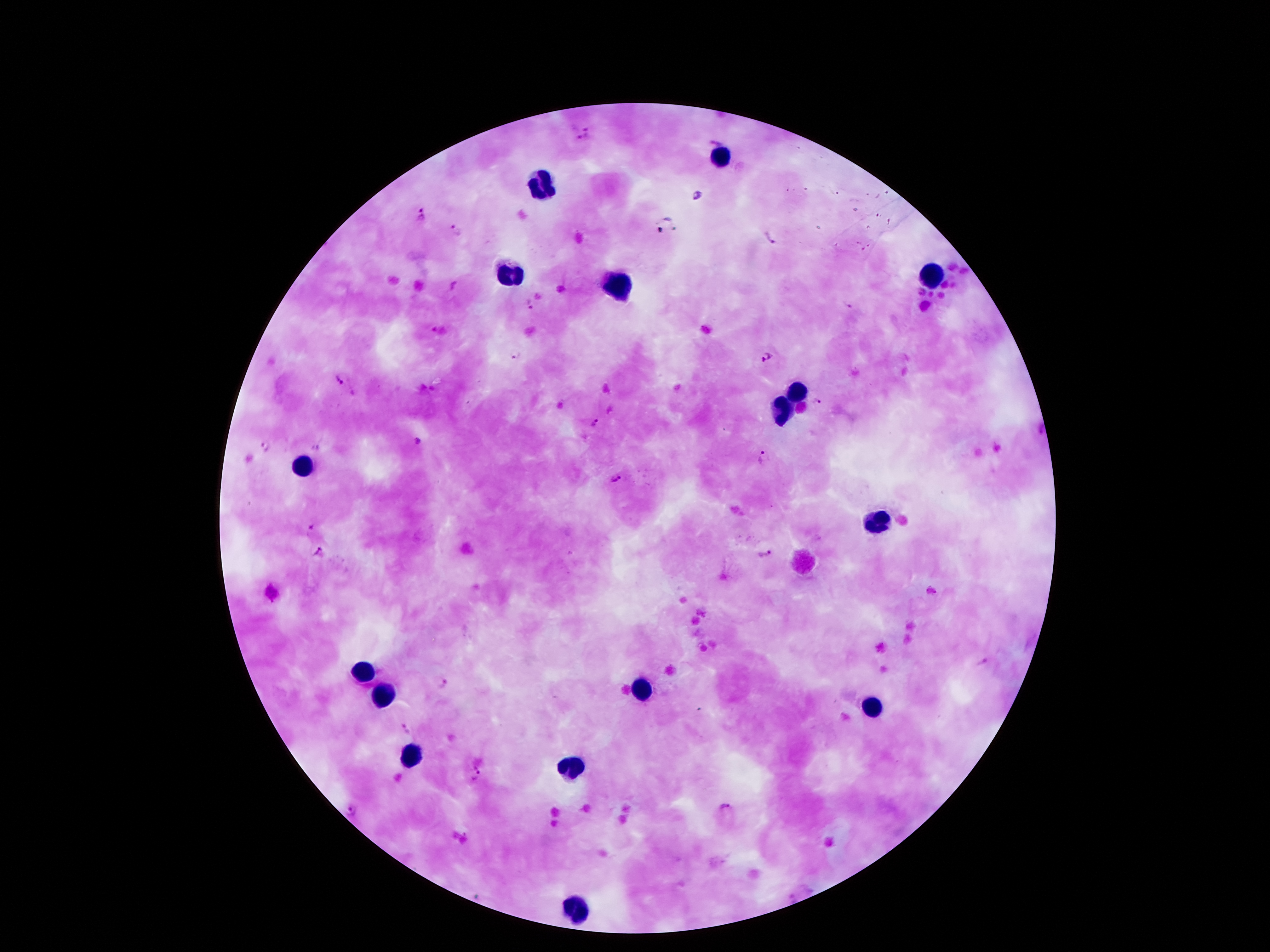
Approximate centers as (x, y) in pixels. Malaria parasite locations: (590, 131), (574, 134), (716, 141), (697, 197), (421, 216), (456, 232), (769, 239), (454, 284), (529, 305), (847, 306), (514, 355), (767, 359), (339, 380), (816, 404), (596, 424), (417, 443), (265, 447), (761, 458), (616, 480), (310, 532), (321, 552), (766, 552), (983, 662), (443, 682), (406, 729), (476, 772), (725, 806), (353, 811). Leukocyte locations: (723, 156), (543, 187), (510, 271), (932, 279), (613, 288), (797, 390), (781, 409), (305, 466), (875, 523), (365, 673), (641, 689), (379, 696), (875, 706), (570, 769), (574, 907). 100x magnification. Smartphone photograph taken through the microscope eyepiece. Single field of view. Patient malaria status: positive for Plasmodium falciparum. Image is 1270×952 pixels. Giemsa-stained preparation. Thick peripheral-blood smear.